State which cell type is depicted.
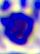
This is a leukocyte.

magnification = 400x
modality = photomicrograph